Identify the blood parasite species.
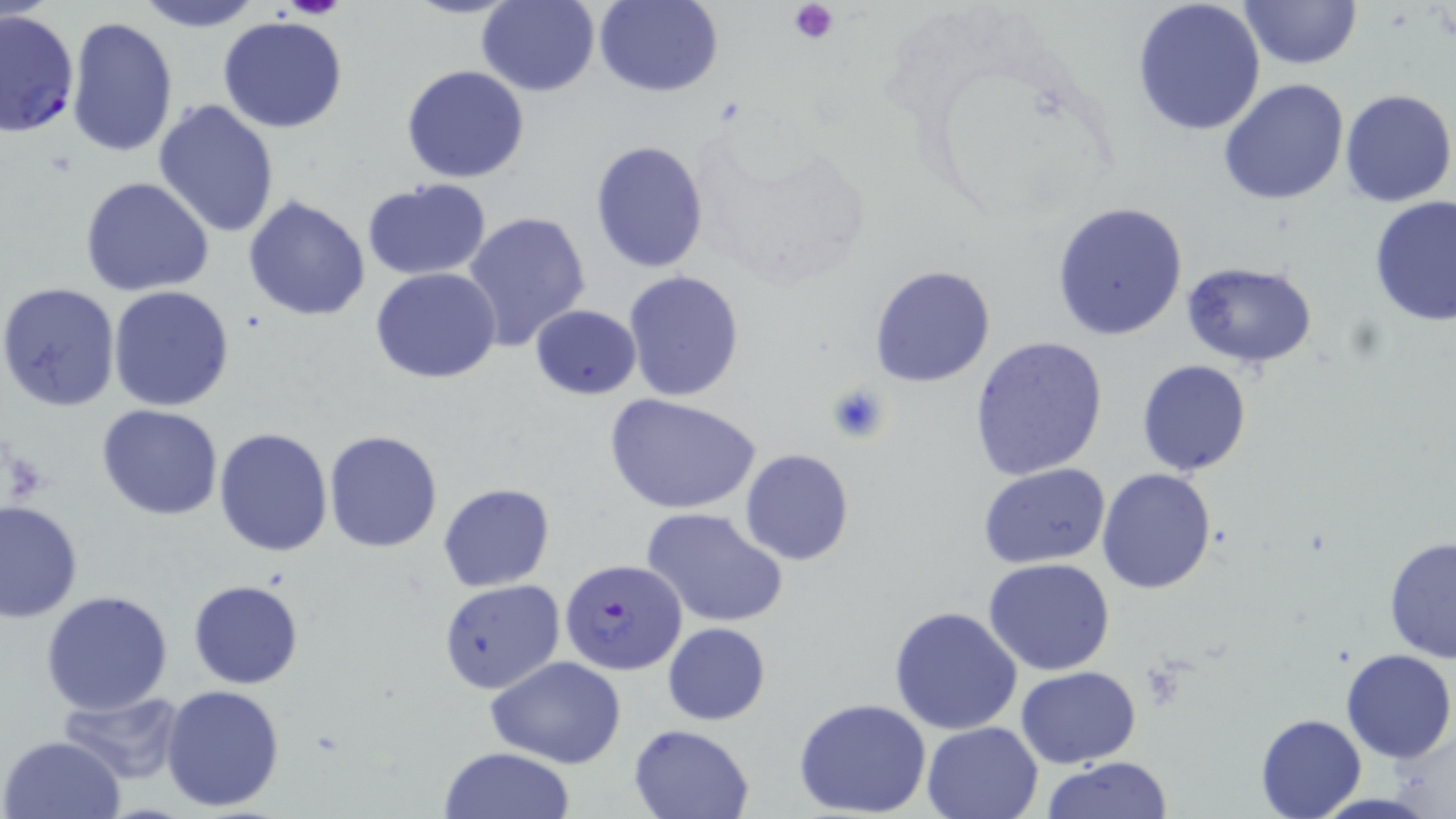
Plasmodium falciparum.

field of view = single
uninfected red blood cell locations = approximate bounding boxes as [x1, y1, x2, y2] in pixels: [133, 0, 264, 32], [403, 0, 520, 19], [477, 0, 600, 96], [594, 0, 724, 97], [1131, 0, 1267, 137], [1240, 1, 1361, 70], [216, 16, 349, 133], [65, 17, 180, 159], [402, 65, 530, 184], [1218, 79, 1351, 206], [1339, 89, 1455, 207], [151, 98, 280, 238], [590, 140, 709, 271], [80, 177, 215, 296], [361, 179, 491, 279], [242, 195, 371, 320], [1369, 195, 1455, 326], [1049, 202, 1188, 340], [462, 210, 590, 353], [1179, 261, 1320, 366], [869, 263, 997, 388], [371, 268, 503, 384], [624, 270, 744, 401], [0, 282, 122, 412], [108, 286, 235, 412], [531, 304, 642, 400], [968, 335, 1109, 481], [1135, 359, 1251, 477], [606, 392, 761, 516], [97, 404, 222, 519], [213, 426, 335, 557], [323, 429, 445, 553], [740, 449, 854, 566], [978, 463, 1109, 566], [1097, 468, 1217, 594], [438, 483, 554, 592], [1, 500, 83, 621], [643, 507, 789, 628], [1384, 536, 1456, 665], [983, 556, 1116, 676], [188, 578, 304, 689], [438, 578, 564, 694], [41, 591, 174, 715], [888, 605, 1024, 736], [662, 622, 770, 724], [1340, 647, 1455, 763], [487, 657, 626, 768], [1016, 666, 1140, 767], [159, 683, 286, 812], [61, 691, 191, 783], [791, 698, 934, 818], [1255, 713, 1364, 819], [920, 721, 1044, 819], [628, 724, 755, 819], [1, 735, 127, 819], [437, 747, 575, 819], [1041, 757, 1173, 819]
platelet locations = approximate bounding boxes as [x1, y1, x2, y2] in pixels: [284, 0, 343, 18], [787, 0, 840, 43], [828, 381, 891, 444]
preparation = thin blood smear
modality = light microscopy
Plasmodium falciparum-infected red blood cell locations = approximate bounding boxes as [x1, y1, x2, y2] in pixels: [0, 9, 79, 139], [560, 557, 687, 677]
image size = 1456×819 pixels
stain = May-Grünwald-Giemsa
magnification = 1000x